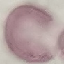

Summary:
  - Result: negative for malaria parasites
  - Capture: smartphone through the microscope eyepiece
  - Image type: cell patch, automatically extracted from a larger field of view and resized to 64 × 64 pixels
  - Stain: Giemsa
  - Preparation: thin smear